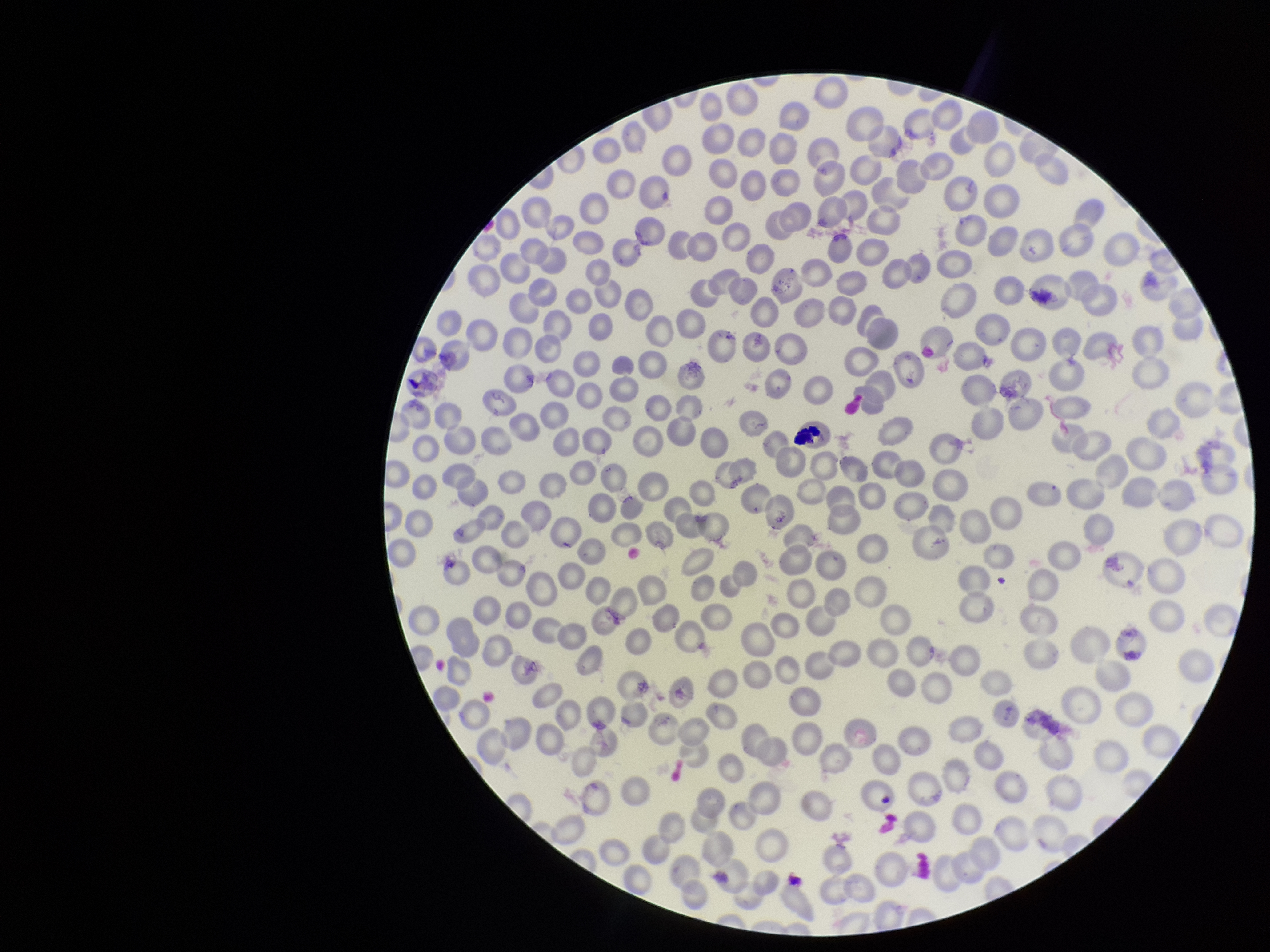
Summary:
  - Field of view: single
  - Parasitized red blood cell count: 0
  - Stain: Giemsa
  - Parasitized red blood cells: none seen
  - Capture: smartphone photograph through the microscope eyepiece
  - Image size: 1270×952 pixels
  - Species reported for this patient: Plasmodium falciparum
  - Patient malaria status: positive
  - Preparation: thin
  - Red blood cell count: 287